Locate and identify every blood parasite.
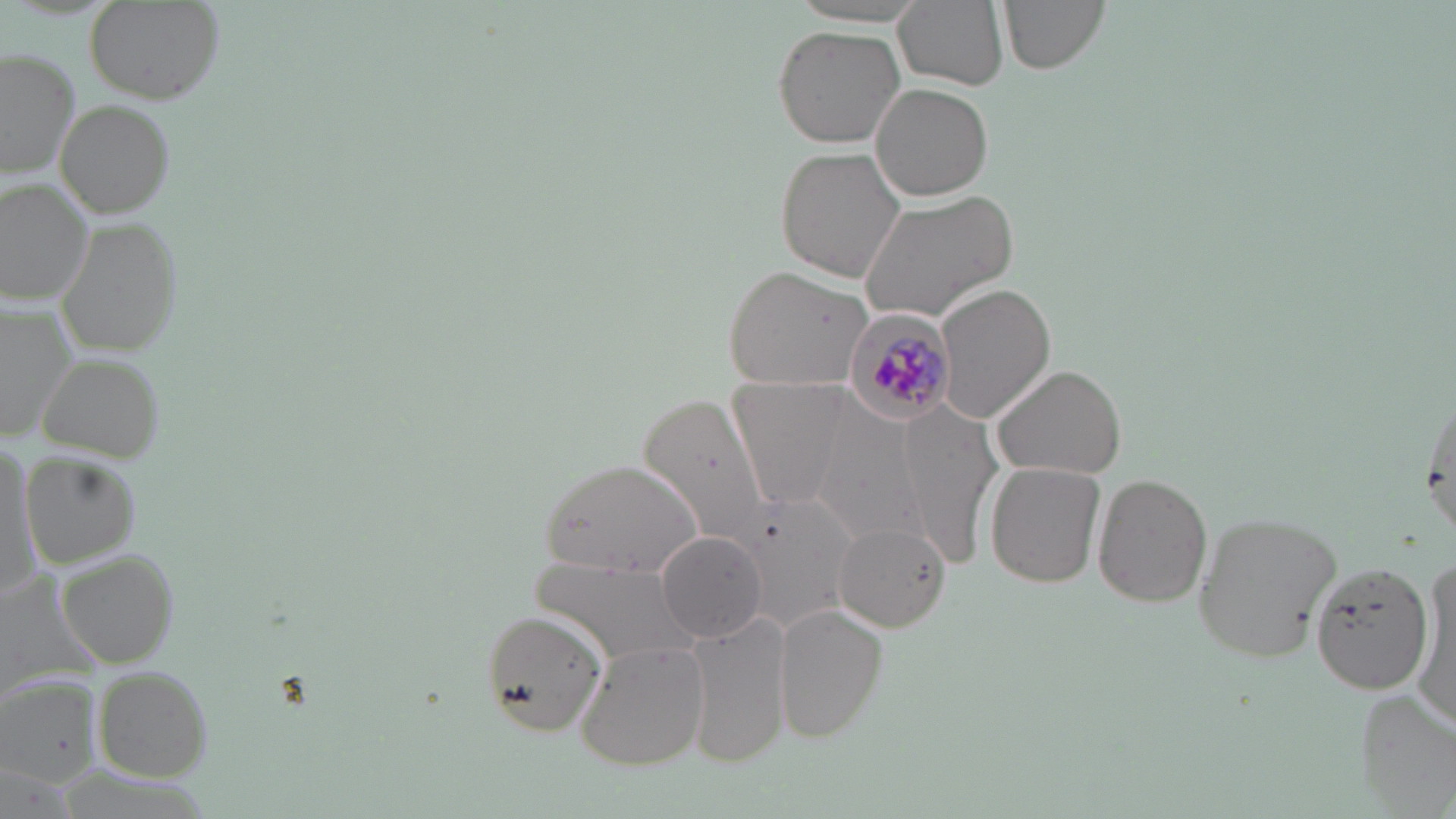
Approximate bounding boxes as (x1,y1)-(x2,y2) corner pairs in pixels.
Plasmodium malariae-infected red blood cells: (843,304)-(956,425).
No Plasmodium falciparum, Plasmodium ovale, Plasmodium vivax, Babesia divergens, or Trypanosoma brucei observed.

{
  "slide_level_diagnosis": "Plasmodium malariae",
  "stain": "May-Grünwald-Giemsa",
  "modality": "light microscopy",
  "magnification": "1000x",
  "field_of_view": "one of a larger specimen",
  "uninfected_red_blood_cell_locations": "approximate bounding boxes as (x1,y1)-(x2,y2) corner pairs in pixels: (895,0)-(1011,93), (997,0)-(1110,73), (84,1)-(222,105), (774,24)-(905,148), (0,47)-(80,181), (873,82)-(994,202), (56,101)-(177,219), (779,147)-(911,282), (0,179)-(96,302), (860,190)-(1017,320), (62,215)-(182,359), (723,265)-(874,390), (934,284)-(1054,424), (0,300)-(80,448), (38,351)-(166,461), (992,362)-(1129,479), (731,379)-(851,508), (1418,382)-(1455,544), (636,391)-(780,552), (898,398)-(1005,555), (817,412)-(919,536), (0,440)-(39,601), (26,452)-(145,567), (542,458)-(708,578), (985,462)-(1106,589), (1092,472)-(1213,610), (731,488)-(859,630), (1192,511)-(1344,662), (834,523)-(950,632), (657,530)-(769,642), (56,546)-(181,668), (528,555)-(700,669), (1414,556)-(1455,731), (1307,557)-(1435,696), (775,606)-(886,743), (480,608)-(608,735), (689,612)-(787,771), (575,641)-(710,771), (89,665)-(215,783), (0,676)-(102,789), (1358,691)-(1456,814)",
  "preparation": "thin blood film",
  "image_size": "1456×819 pixels"
}